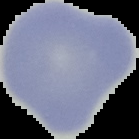

The area outside the segmented cell region is set to black. Malaria status: uninfected. Image is 139×139 pixels. From a thin blood smear.